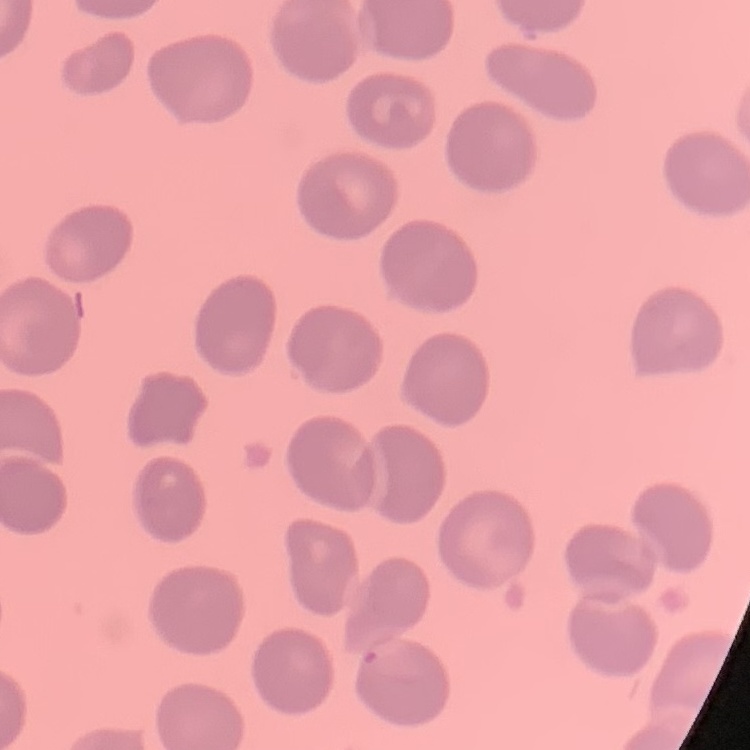
erythrocyte_morphology: no rouleaux formation
preparation: thin blood film
stain: Field's or Giemsa
image_type: square crop of a larger photomicrograph